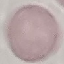 Result: no malaria parasites seen. Acquired by smartphone through the microscope eyepiece. Giemsa-stained preparation. Cell patch, automatically extracted from a larger field of view and resized to 64 × 64 pixels. Thin blood smear.